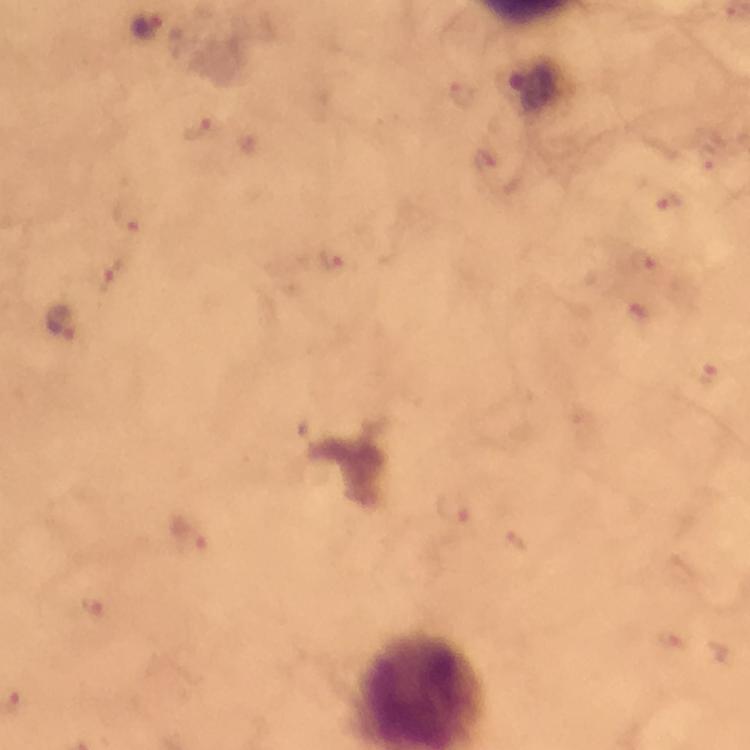
Approximate centers as [x, y] in pixels.
Summary:
  - Malaria parasite locations: [148, 25], [462, 95], [199, 129], [709, 156], [668, 201], [129, 215], [332, 257], [645, 260], [110, 275], [62, 323], [709, 375], [454, 508], [189, 535], [514, 542], [92, 605], [668, 640], [721, 650]
  - Context: from a malaria diagnostic workup
  - Cropped from: a single field of view
  - Preparation: thick smear
  - Stain: Giemsa
  - Immersion oil: used
  - Magnification: 100x
  - Image size: 750×750 pixels
  - Capture: smartphone mounted on the microscope